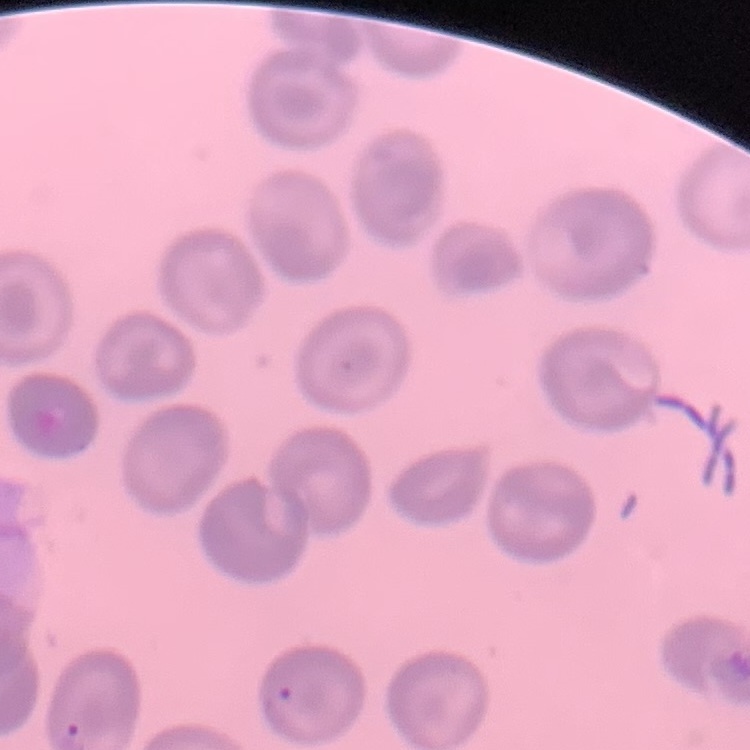 The erythrocytes show no rouleaux formation. One tile cut from a larger photomicrograph. Thin blood smear. Field's or Giemsa stain.